Assess the morphology of the red blood cells.
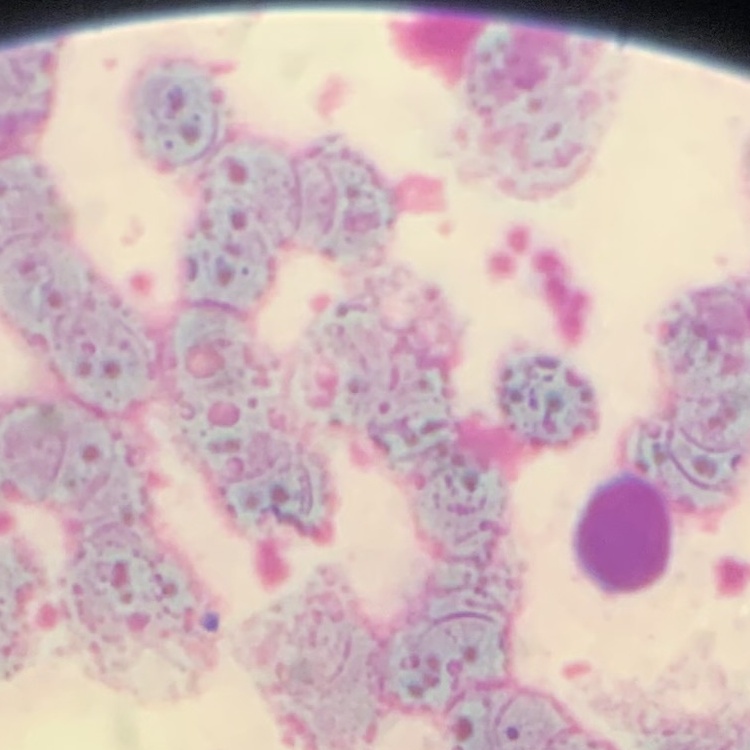
Rouleaux formation.

Summary:
  - Preparation: thin peripheral smear
  - Stain: Field's or Giemsa
  - Image type: one tile cut from a larger photomicrograph